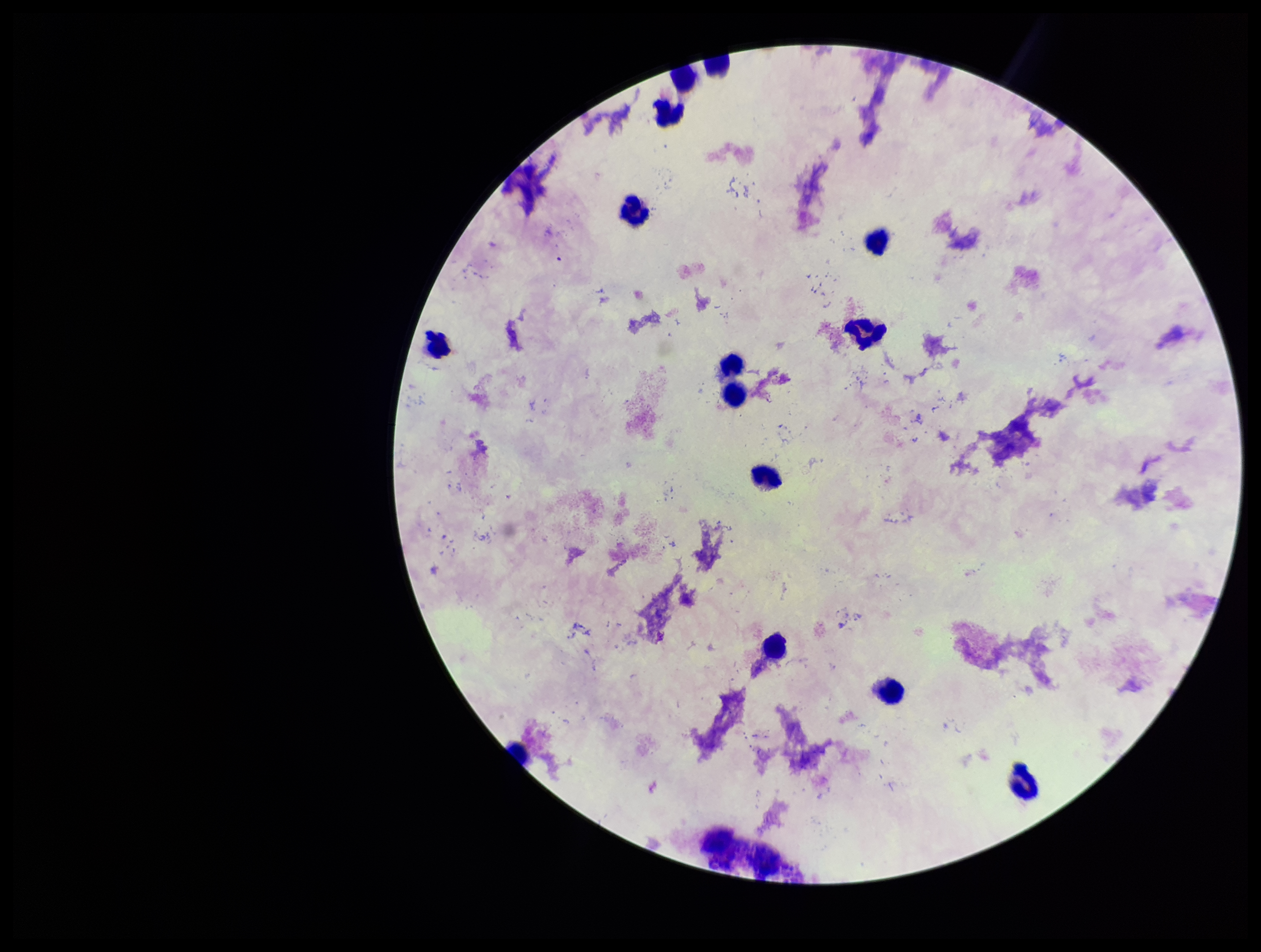
Summary:
  - Stain: Giemsa
  - Patient malaria status: negative
  - Preparation: thick
  - Field of view: one from this slide
  - Image size: 1261×952 pixels
  - Capture: smartphone photograph through the microscope eyepiece
  - Parasite count: 0
  - Leukocyte count: 13
  - Plasmodium parasites: none detected